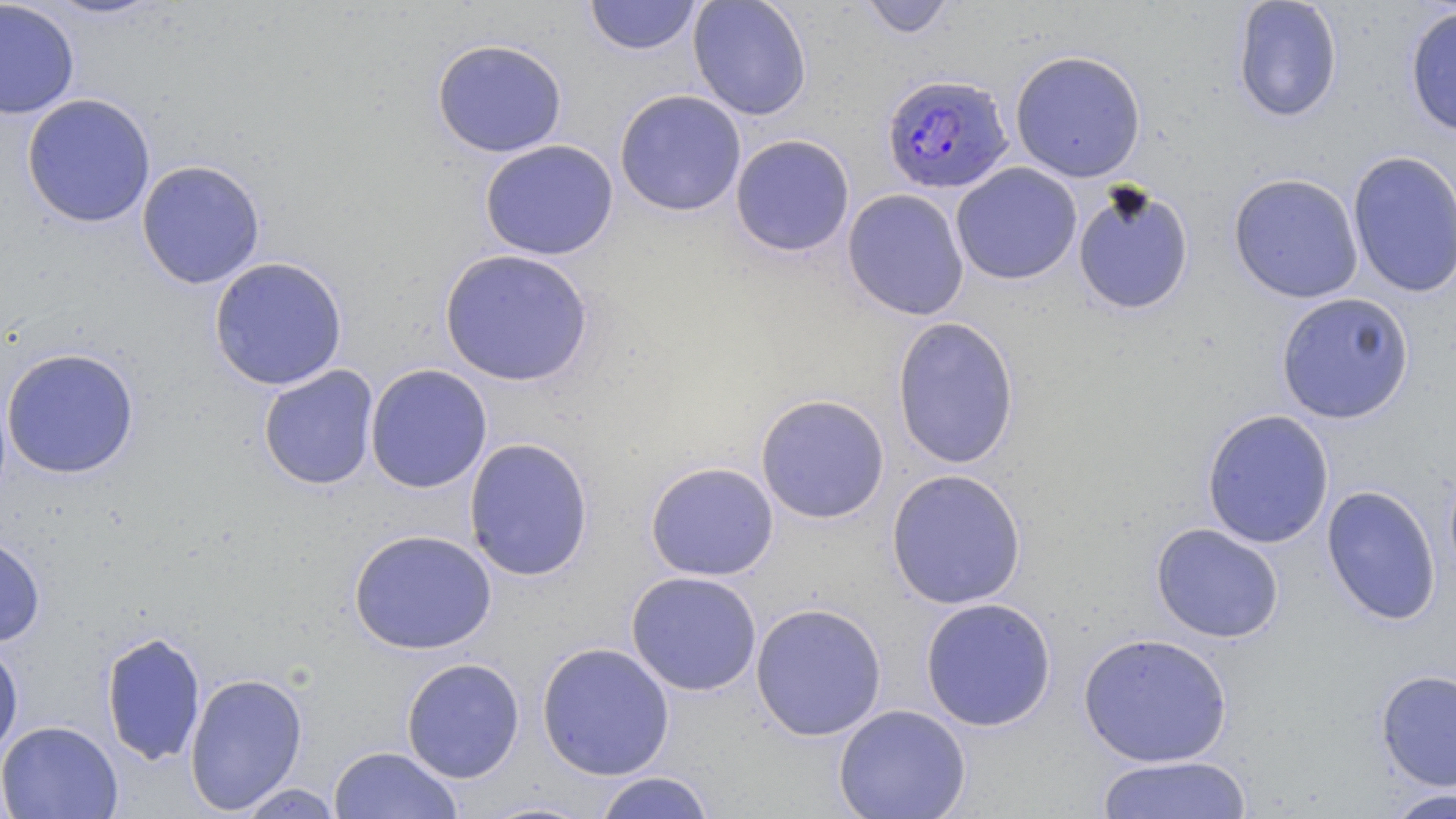

{
  "slide_level_diagnosis": "Plasmodium falciparum",
  "image_size": "1456×819 pixels",
  "modality": "optical microscopy",
  "magnification": "1000x",
  "stain": "May-Grünwald-Giemsa",
  "preparation": "thin blood smear",
  "uninfected_red_blood_cell_locations": "approximate bounding boxes as [x1, y1, x2, y2] in pixels: [0, 0, 79, 119], [39, 0, 166, 20], [584, 0, 701, 56], [688, 0, 812, 120], [858, 0, 956, 39], [1232, 0, 1343, 123], [1404, 5, 1456, 138], [431, 38, 568, 158], [1009, 49, 1146, 183], [614, 89, 747, 217], [21, 93, 156, 228], [730, 134, 855, 258], [479, 139, 619, 260], [1346, 150, 1456, 298], [136, 159, 266, 289], [951, 162, 1082, 285], [1228, 172, 1363, 303], [1073, 183, 1195, 316], [842, 188, 969, 320], [439, 248, 594, 386], [208, 256, 348, 391], [1276, 292, 1415, 424], [891, 316, 1021, 470], [1, 347, 139, 478], [365, 363, 492, 493], [258, 365, 379, 490], [755, 393, 890, 524], [1201, 409, 1334, 548], [463, 437, 594, 582], [645, 461, 779, 581], [886, 468, 1026, 610], [1321, 485, 1441, 626], [1150, 522, 1285, 643], [348, 528, 497, 655], [0, 532, 46, 646], [626, 570, 762, 696], [919, 597, 1057, 732], [750, 601, 887, 741], [100, 630, 206, 766], [1078, 632, 1233, 766], [0, 638, 23, 762], [535, 641, 675, 781], [401, 657, 525, 783], [1375, 669, 1456, 791], [184, 671, 308, 814], [833, 703, 971, 819], [0, 720, 123, 819], [328, 745, 464, 819], [1096, 754, 1253, 818], [592, 771, 716, 819], [234, 783, 346, 818], [1382, 787, 1456, 819]",
  "field_of_view": "single",
  "plasmodium_falciparum_infected_red_blood_cell_locations": "approximate bounding boxes as [x1, y1, x2, y2] in pixels: [881, 73, 1014, 194]"
}